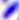 400x magnification. Toxoplasma gondii is shown. Micrograph.